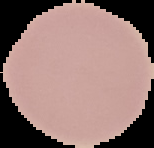
Result: no malaria parasites seen. Image is 154×148 pixels. From a thin blood smear. Cell region segmented out of the field of view; the surrounding area is masked to black.